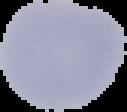 From a thin blood film. The area outside the segmented cell region is set to black. Result: negative for Plasmodium parasites. Image is 127×112 pixels.